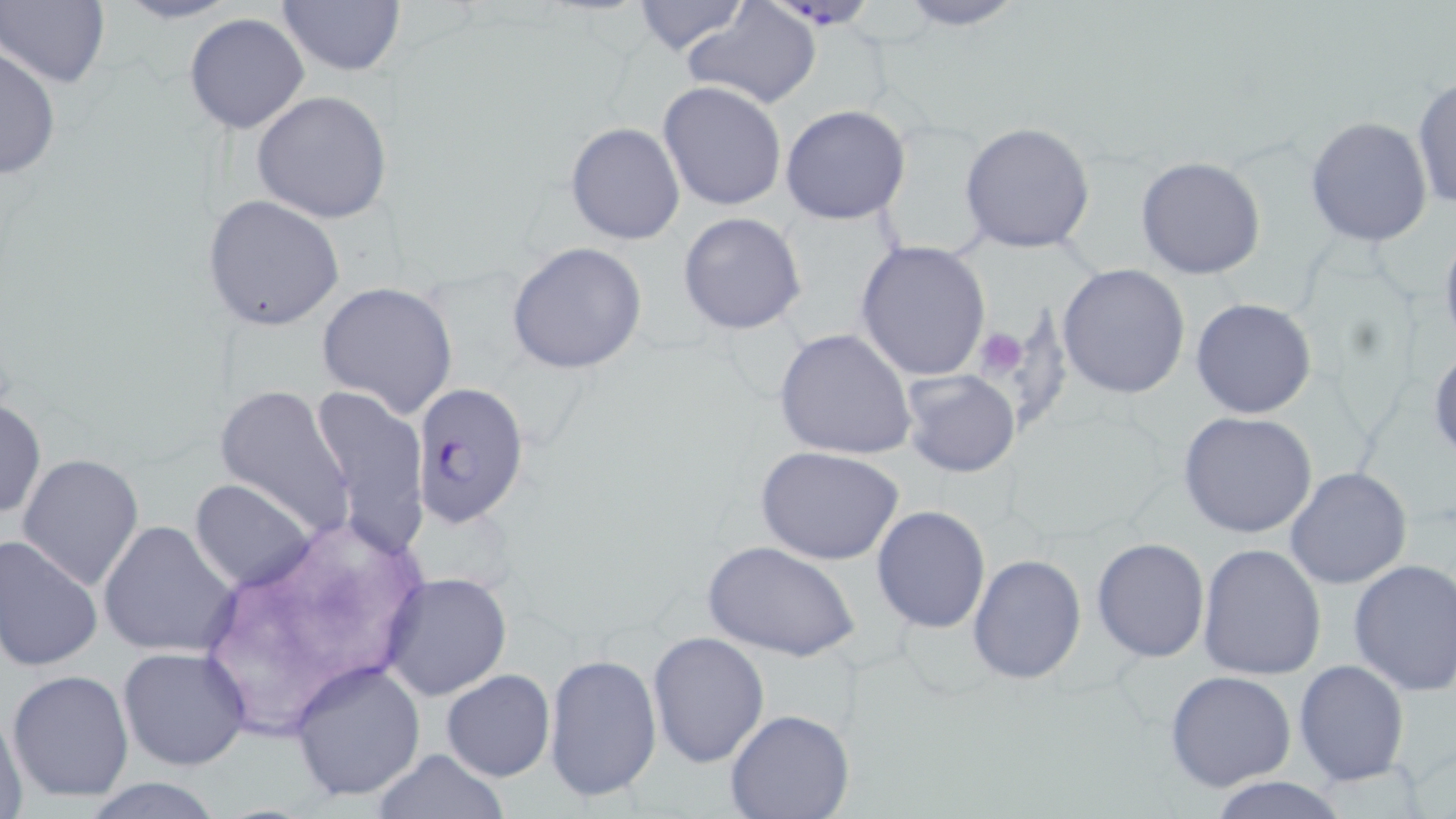 Approximate bounding boxes as [x1, y1, x2, y2] in pixels. Uninfected red blood cell locations: [107, 0, 245, 25], [890, 0, 1032, 31], [0, 1, 110, 88], [630, 1, 751, 57], [276, 2, 405, 78], [680, 2, 823, 109], [183, 13, 310, 134], [1, 44, 62, 179], [1412, 75, 1455, 215], [657, 81, 787, 212], [251, 91, 393, 225], [780, 104, 912, 225], [1305, 115, 1434, 247], [958, 121, 1099, 252], [567, 122, 685, 246], [1136, 156, 1266, 280], [202, 194, 345, 332], [679, 212, 805, 334], [1438, 222, 1456, 352], [856, 240, 991, 380], [506, 243, 647, 375], [1057, 263, 1190, 400], [316, 281, 459, 418], [1191, 298, 1318, 420], [773, 328, 916, 463], [1428, 345, 1456, 462], [900, 368, 1020, 477], [212, 382, 355, 536], [309, 384, 431, 556], [0, 395, 46, 522], [1177, 410, 1317, 538], [755, 445, 904, 566], [16, 453, 146, 591], [1284, 466, 1413, 590], [189, 478, 317, 593], [871, 506, 991, 634], [98, 520, 241, 660], [0, 534, 103, 672], [1091, 537, 1210, 662], [702, 540, 858, 663], [1197, 545, 1327, 683], [967, 554, 1087, 684], [1347, 559, 1456, 697], [379, 572, 513, 700], [647, 632, 769, 768], [117, 645, 252, 773], [544, 652, 663, 806], [288, 658, 425, 802], [1293, 660, 1409, 786], [7, 667, 134, 804], [440, 669, 555, 781], [1164, 671, 1297, 792], [0, 701, 28, 816], [724, 710, 855, 819], [371, 747, 510, 819], [1205, 775, 1352, 819], [80, 779, 229, 817]. Platelet locations: [973, 327, 1030, 380]. Plasmodium falciparum-infected red blood cell locations: [783, 0, 874, 39], [408, 379, 531, 530]. Slide-level diagnosis: Plasmodium falciparum. May-Grünwald-Giemsa stain. One field of a larger specimen. Image is 1456×819 pixels. 1000x magnification. Thin blood film. Optical microscopy.